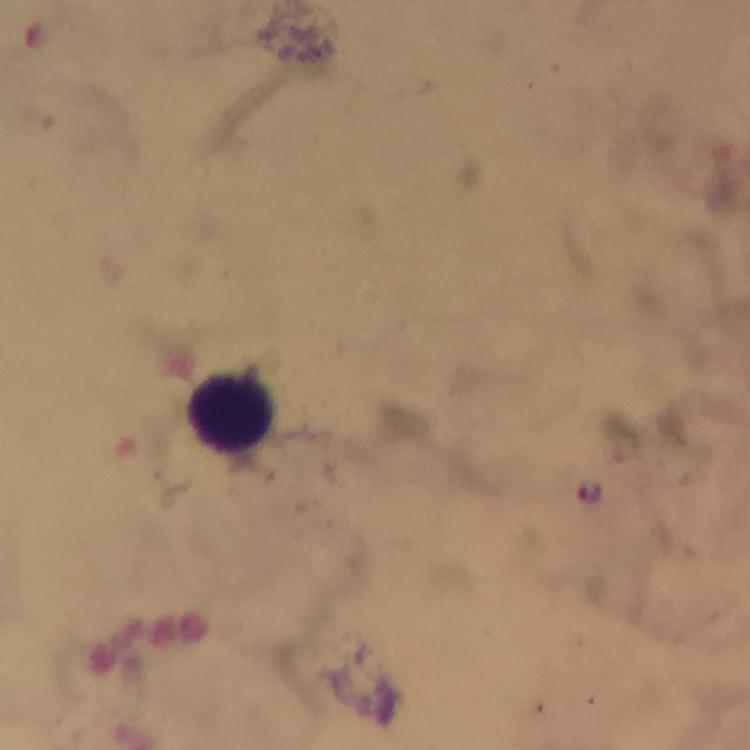

magnification = 100x
image size = 750×750 pixels
cropped from = a single field of view
capture = smartphone camera through the microscope
stain = Giemsa
context = from a diagnostic examination for malaria
immersion oil = applied
preparation = thick smear
malaria parasite locations = approximate object centers, in pixels from the top-left corner: (x=591, y=493)
leukocyte locations = approximate object centers, in pixels from the top-left corner: (x=237, y=408)